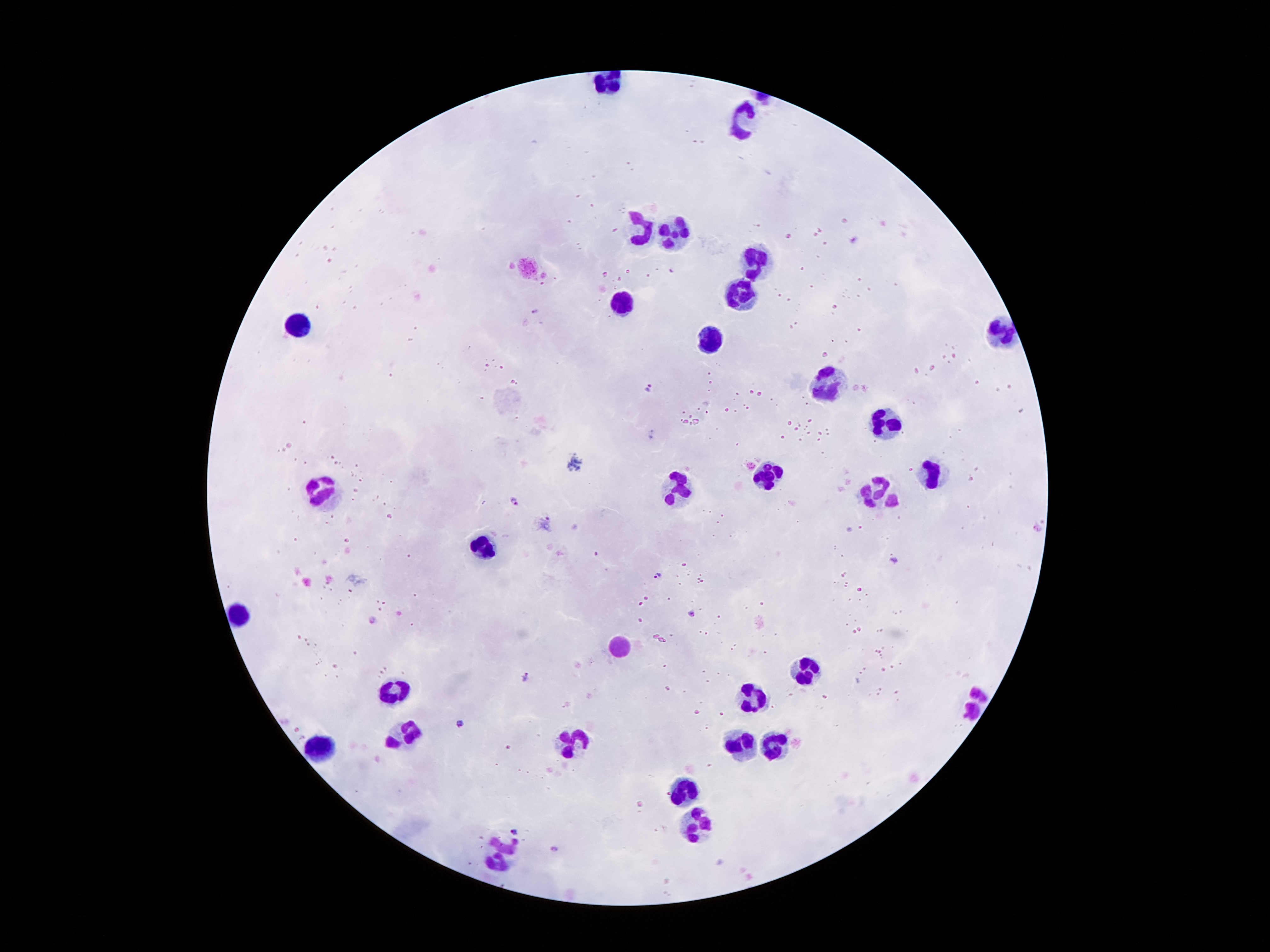 Approximate centers as {x, y} in pixels. Leukocyte locations: {744, 119}, {673, 229}, {645, 231}, {754, 263}, {625, 302}, {300, 321}, {998, 332}, {705, 347}, {836, 382}, {888, 427}, {767, 472}, {933, 479}, {326, 489}, {677, 489}, {879, 489}, {485, 545}, {235, 614}, {617, 646}, {804, 668}, {397, 683}, {748, 698}, {974, 707}, {403, 733}, {571, 741}, {739, 741}, {772, 745}, {322, 748}, {681, 789}, {692, 823}, {500, 851}. Malaria parasite locations: {856, 240}, {671, 272}, {534, 311}, {648, 387}, {652, 433}, {516, 502}, {547, 524}, {893, 560}, {658, 575}, {691, 613}, {372, 620}, {527, 677}, {461, 723}, {515, 832}, {554, 849}. 100x magnification. Single field of view. Giemsa stain. Image is 1270×952 pixels. Patient malaria status: positive for Plasmodium falciparum. Smartphone photograph taken through the microscope eyepiece. Thick blood film.